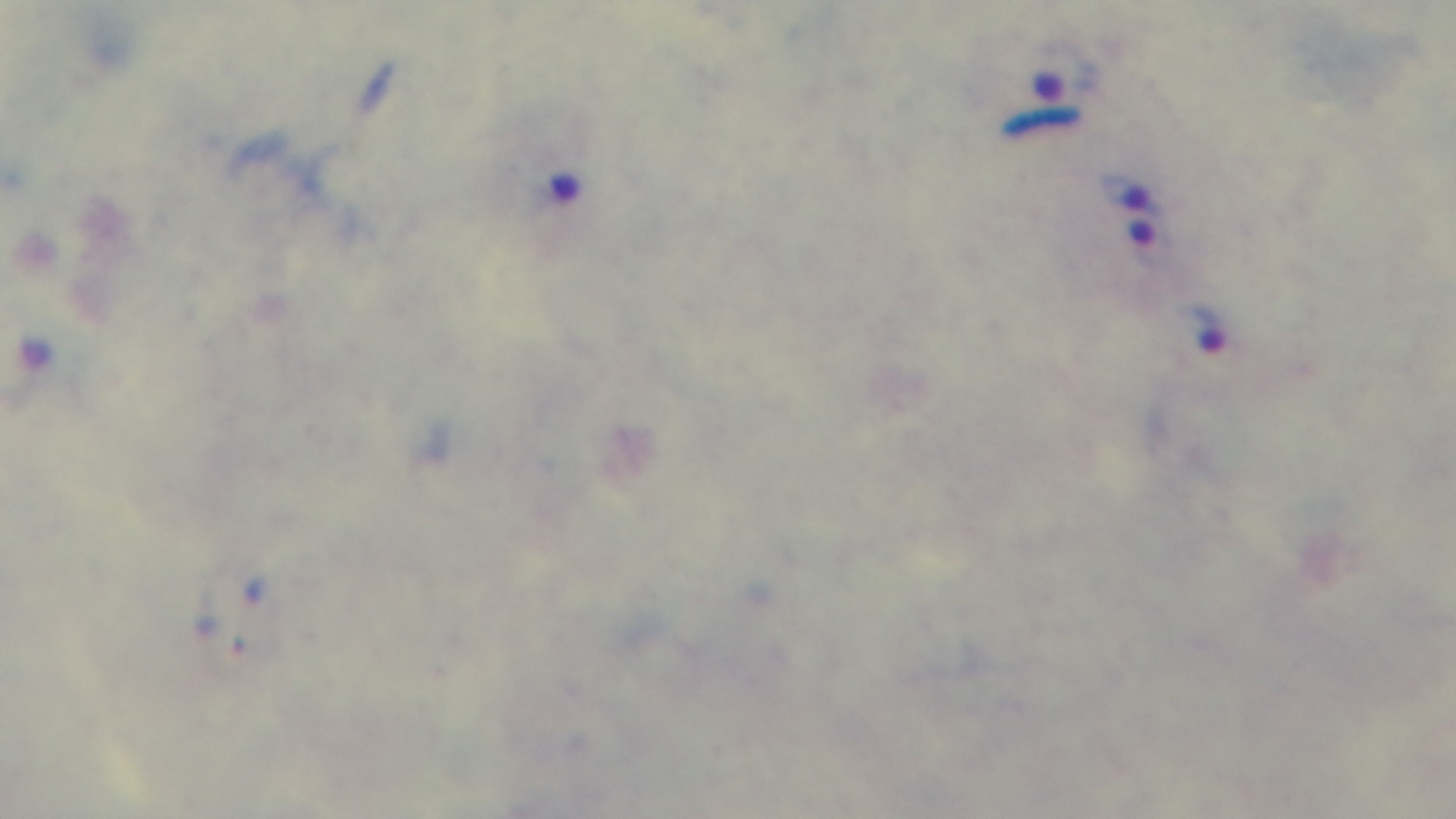

preparation = thick blood film
malaria status = infected
objective = 100x oil immersion
capture = mounted 4K digital camera
field of view = one from the slide
modality = light microscopy
stain = Giemsa